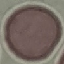
Summary:
  - Result: no malaria parasites seen
  - Image type: automatically extracted cell patch, resized to 64 × 64 pixels
  - Stain: Giemsa
  - Capture: smartphone through the microscope eyepiece
  - Preparation: thin blood smear